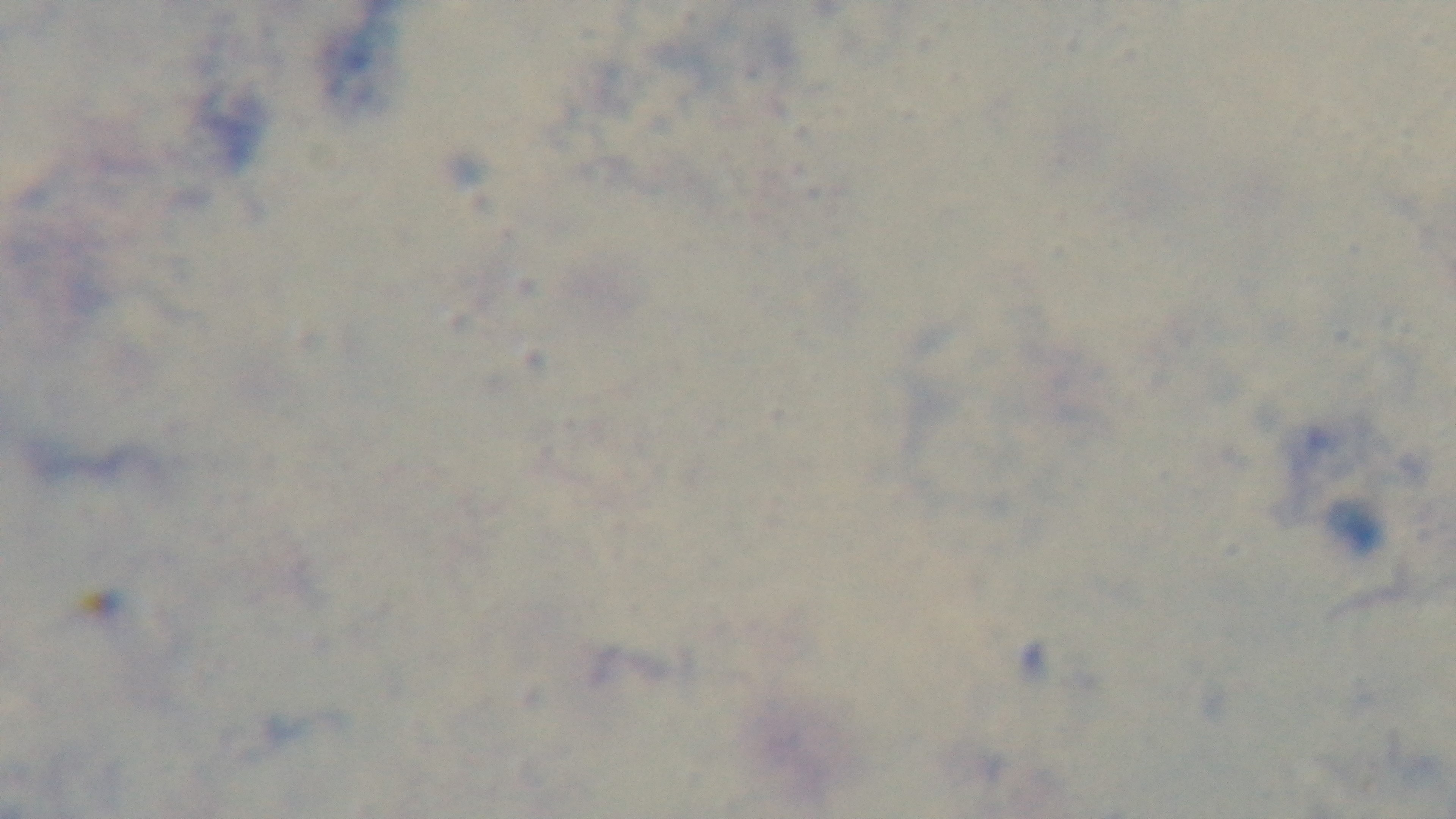
Preparation: thick smear. 100x oil-immersion objective. Photomicrograph. Giemsa-stained. Mounted 4K digital camera. One field from the slide. Malaria status: negative.